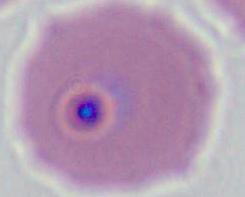

Summary:
  - Identification: Plasmodium
  - Modality: micrograph
  - Magnification: 400x or 1000x